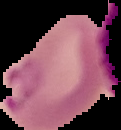

Image is 121×130 pixels. Segmented cell region on a black background. Result: Plasmodium parasites detected. From a thin blood film.